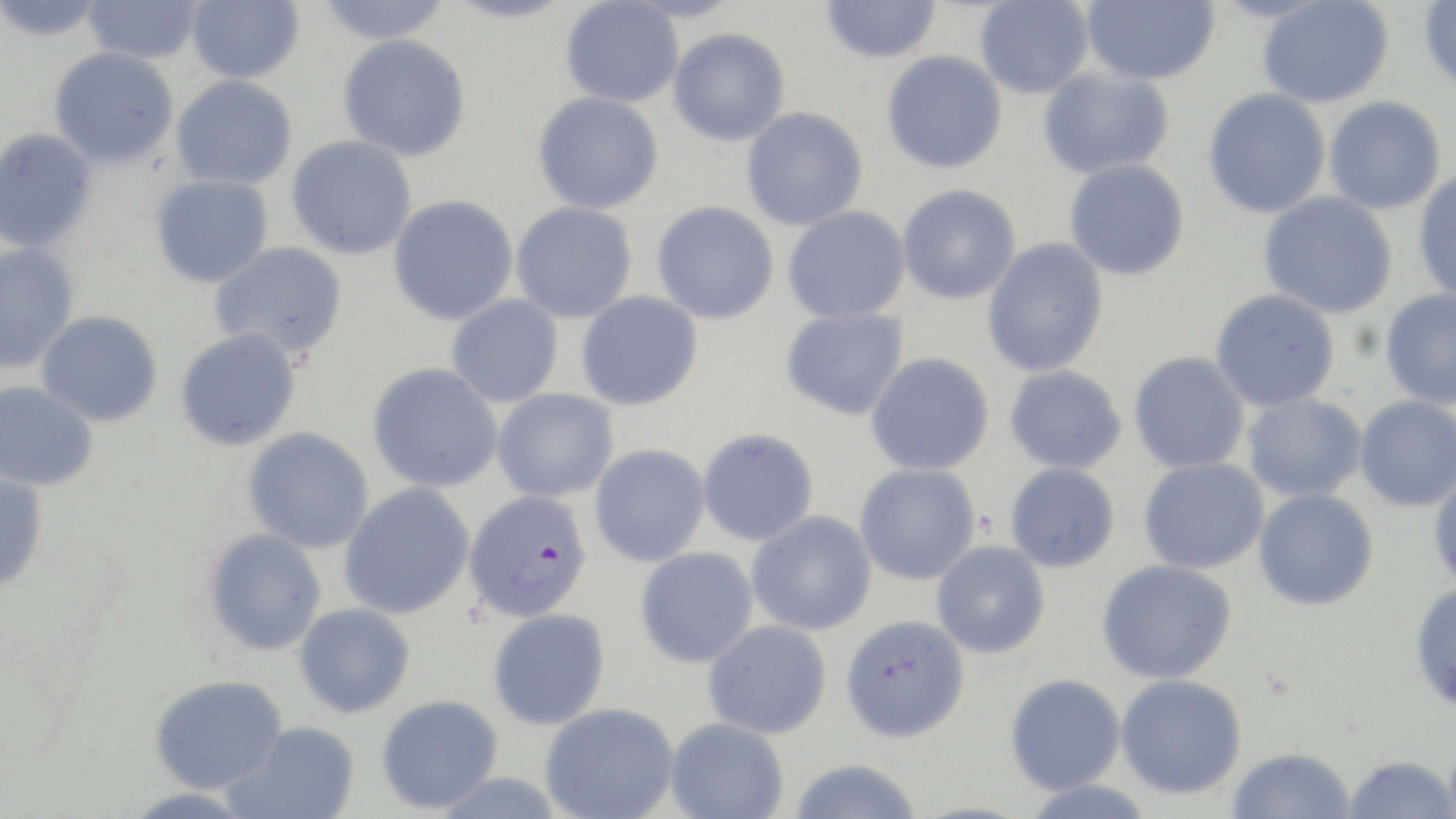

{
  "plasmodium_falciparum_infected_red_blood_cell_locations": "approximate bounding boxes as named x1/y1/x2/y2 corners in pixels: (x1=463, y1=489, x2=593, y2=621)",
  "slide_level_diagnosis": "Plasmodium falciparum",
  "modality": "optical microscopy",
  "magnification": "1000x",
  "uninfected_red_blood_cell_locations": "approximate bounding boxes as named x1/y1/x2/y2 corners in pixels: (x1=1, y1=0, x2=108, y2=42), (x1=82, y1=0, x2=204, y2=64), (x1=186, y1=0, x2=304, y2=84), (x1=314, y1=0, x2=453, y2=45), (x1=445, y1=0, x2=575, y2=24), (x1=820, y1=0, x2=942, y2=64), (x1=974, y1=0, x2=1093, y2=100), (x1=1081, y1=0, x2=1220, y2=86), (x1=560, y1=1, x2=684, y2=108), (x1=1256, y1=1, x2=1393, y2=108), (x1=1419, y1=1, x2=1456, y2=93), (x1=667, y1=28, x2=790, y2=146), (x1=338, y1=34, x2=471, y2=161), (x1=48, y1=46, x2=180, y2=168), (x1=881, y1=50, x2=1007, y2=174), (x1=1037, y1=67, x2=1175, y2=179), (x1=170, y1=75, x2=297, y2=189), (x1=1202, y1=88, x2=1331, y2=219), (x1=532, y1=92, x2=664, y2=215), (x1=1324, y1=96, x2=1446, y2=214), (x1=741, y1=106, x2=868, y2=231), (x1=0, y1=128, x2=99, y2=253), (x1=286, y1=135, x2=418, y2=260), (x1=1064, y1=158, x2=1190, y2=281), (x1=1413, y1=170, x2=1456, y2=304), (x1=149, y1=174, x2=274, y2=288), (x1=896, y1=183, x2=1022, y2=305), (x1=1258, y1=192, x2=1398, y2=319), (x1=388, y1=195, x2=519, y2=326), (x1=651, y1=201, x2=780, y2=325), (x1=510, y1=202, x2=638, y2=324), (x1=783, y1=205, x2=911, y2=323), (x1=981, y1=237, x2=1109, y2=377), (x1=209, y1=241, x2=349, y2=361), (x1=0, y1=243, x2=80, y2=374), (x1=1209, y1=289, x2=1341, y2=412), (x1=575, y1=290, x2=704, y2=411), (x1=1379, y1=290, x2=1456, y2=409), (x1=446, y1=294, x2=564, y2=408), (x1=781, y1=307, x2=910, y2=421), (x1=36, y1=310, x2=163, y2=427), (x1=175, y1=328, x2=302, y2=451), (x1=1128, y1=351, x2=1251, y2=474), (x1=865, y1=352, x2=995, y2=475), (x1=367, y1=363, x2=503, y2=492), (x1=1004, y1=365, x2=1127, y2=474), (x1=0, y1=380, x2=98, y2=491), (x1=492, y1=389, x2=620, y2=502), (x1=1241, y1=393, x2=1368, y2=503), (x1=1354, y1=395, x2=1456, y2=511), (x1=242, y1=427, x2=374, y2=554), (x1=697, y1=427, x2=820, y2=546), (x1=589, y1=444, x2=711, y2=567), (x1=1138, y1=457, x2=1269, y2=574), (x1=1005, y1=462, x2=1121, y2=573), (x1=854, y1=463, x2=981, y2=586), (x1=1428, y1=469, x2=1456, y2=593), (x1=0, y1=472, x2=48, y2=593), (x1=338, y1=482, x2=475, y2=619), (x1=1253, y1=488, x2=1379, y2=610), (x1=747, y1=511, x2=877, y2=636), (x1=203, y1=527, x2=327, y2=656), (x1=931, y1=540, x2=1051, y2=659), (x1=635, y1=546, x2=758, y2=668), (x1=1096, y1=559, x2=1237, y2=684), (x1=1410, y1=580, x2=1456, y2=712), (x1=294, y1=603, x2=415, y2=717), (x1=488, y1=607, x2=611, y2=730), (x1=840, y1=614, x2=970, y2=743), (x1=702, y1=619, x2=832, y2=739), (x1=1005, y1=673, x2=1126, y2=795), (x1=149, y1=674, x2=286, y2=794), (x1=1115, y1=674, x2=1247, y2=800), (x1=376, y1=694, x2=503, y2=814), (x1=540, y1=702, x2=680, y2=819), (x1=665, y1=717, x2=789, y2=818), (x1=224, y1=721, x2=360, y2=819), (x1=1444, y1=739, x2=1456, y2=819), (x1=1227, y1=747, x2=1356, y2=819), (x1=1342, y1=755, x2=1456, y2=818), (x1=788, y1=758, x2=923, y2=819), (x1=1019, y1=778, x2=1157, y2=819), (x1=117, y1=786, x2=258, y2=817)",
  "preparation": "thin blood film",
  "field_of_view": "single",
  "image_size": "1456×819 pixels",
  "stain": "May-Grünwald-Giemsa"
}